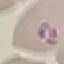

result = malaria parasites identified
stain = Giemsa
image type = cell patch, automatically extracted from a larger field of view and resized to 64 × 64 pixels
capture = smartphone camera at the microscope eyepiece
preparation = thin blood film